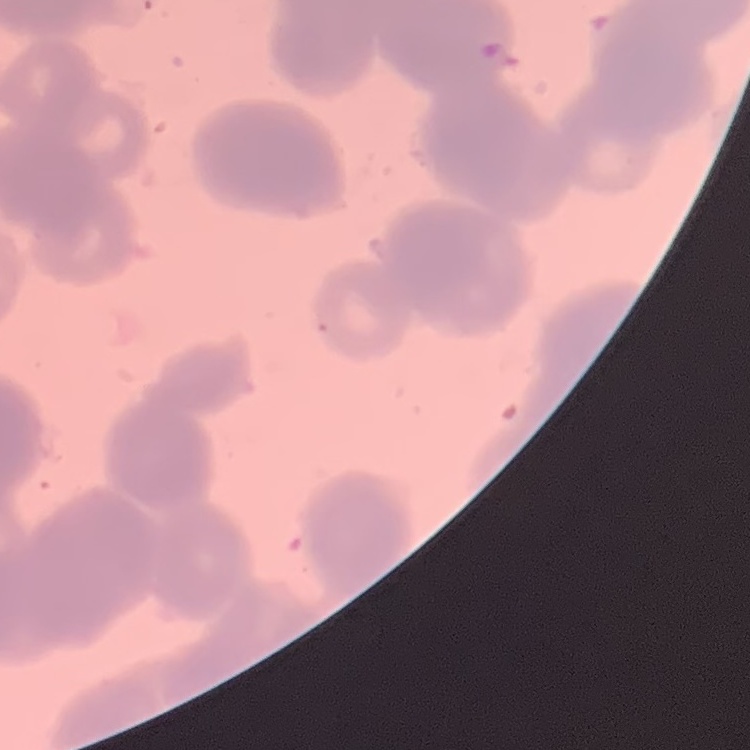

erythrocyte morphology = rouleaux formation
stain = Field's or Giemsa
preparation = thin blood smear
image type = square crop of a larger photomicrograph